State which cell type is depicted.
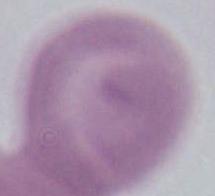
This is an erythrocyte.

magnification = 1000x
modality = photomicrograph